Report the malaria status of this cell.
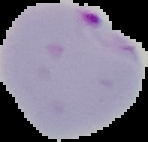
Parasitized.

Image is 148×142 pixels. From a thin blood film. Cell region segmented out of the field of view; the surrounding area is masked to black.